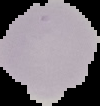
Image is 100×106 pixels. Malaria status: uninfected. From a thin blood smear. Cell region segmented out of the field of view; the surrounding area is masked to black.